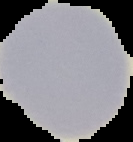
Result: negative for Plasmodium parasites. Image is 133×142 pixels. Segmented cell region on a black background. From a thin blood smear.